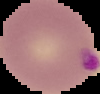

{
  "preparation": "thin blood film",
  "image_size": "100×94 pixels",
  "image_type": "segmented cell region with the area outside set to black",
  "malaria_status": "parasitized"
}